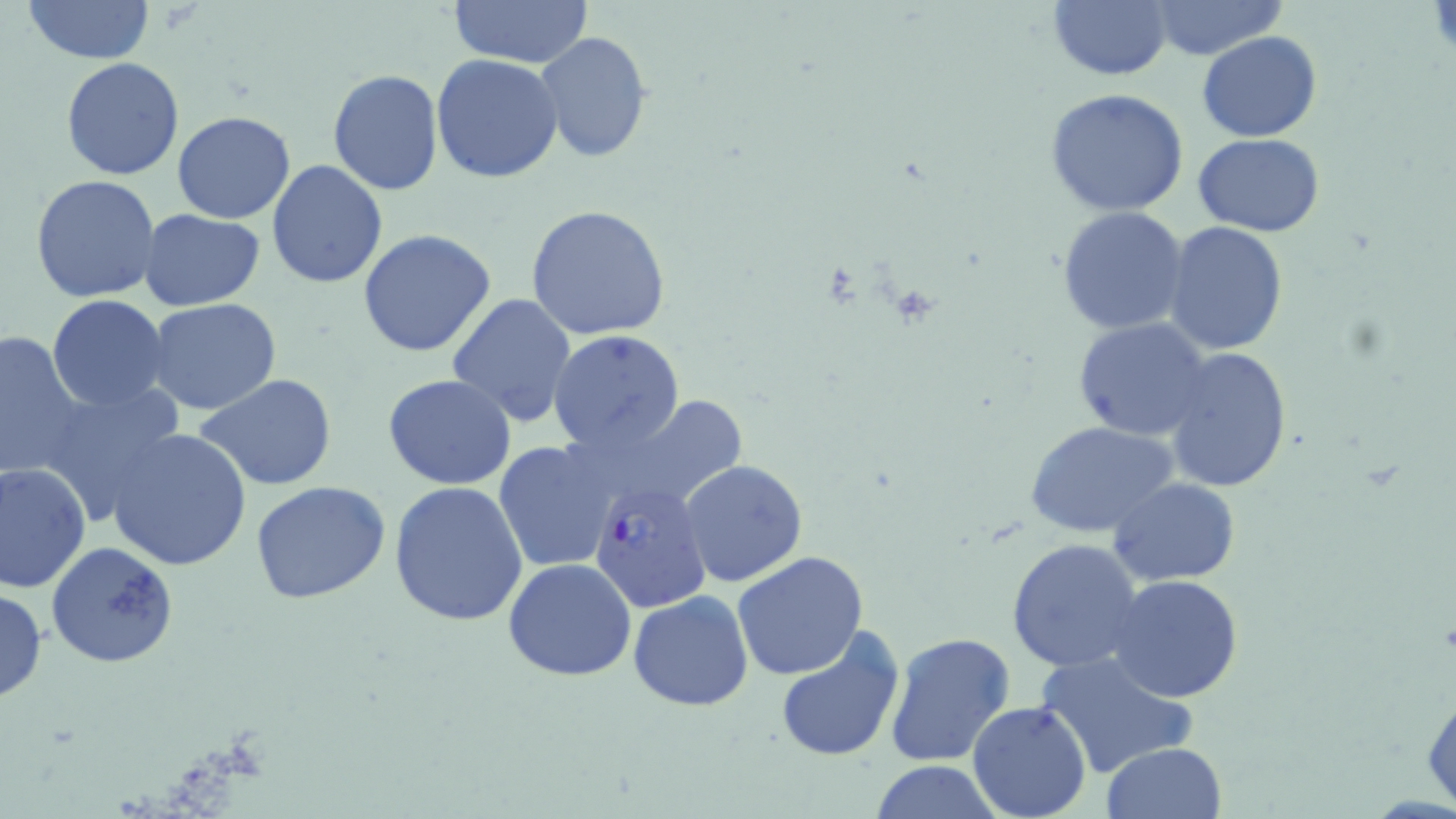

Approximate bounding boxes as named x1/y1/x2/y2 corners in pixels. Plasmodium falciparum-infected red blood cell locations: (x1=588, y1=479, x2=712, y2=614). Uninfected red blood cell locations: (x1=20, y1=0, x2=157, y2=65), (x1=449, y1=0, x2=593, y2=70), (x1=1049, y1=0, x2=1173, y2=81), (x1=1146, y1=3, x2=1283, y2=59), (x1=1197, y1=30, x2=1321, y2=142), (x1=532, y1=32, x2=653, y2=162), (x1=430, y1=53, x2=563, y2=182), (x1=60, y1=57, x2=186, y2=180), (x1=327, y1=69, x2=446, y2=196), (x1=1044, y1=88, x2=1189, y2=216), (x1=172, y1=111, x2=296, y2=224), (x1=1193, y1=133, x2=1324, y2=238), (x1=266, y1=158, x2=388, y2=289), (x1=31, y1=174, x2=162, y2=304), (x1=524, y1=203, x2=672, y2=342), (x1=1055, y1=207, x2=1189, y2=335), (x1=139, y1=208, x2=267, y2=311), (x1=1165, y1=222, x2=1287, y2=355), (x1=357, y1=229, x2=498, y2=357), (x1=446, y1=292, x2=578, y2=426), (x1=47, y1=294, x2=172, y2=413), (x1=146, y1=299, x2=283, y2=417), (x1=1074, y1=317, x2=1214, y2=442), (x1=0, y1=329, x2=88, y2=483), (x1=549, y1=330, x2=685, y2=454), (x1=1163, y1=347, x2=1292, y2=493), (x1=194, y1=373, x2=340, y2=493), (x1=384, y1=374, x2=517, y2=491), (x1=33, y1=378, x2=189, y2=524), (x1=591, y1=395, x2=747, y2=512), (x1=1026, y1=420, x2=1179, y2=539), (x1=107, y1=428, x2=253, y2=572), (x1=493, y1=440, x2=619, y2=574), (x1=679, y1=459, x2=808, y2=587), (x1=0, y1=462, x2=92, y2=593), (x1=1108, y1=478, x2=1242, y2=585), (x1=250, y1=481, x2=392, y2=605), (x1=389, y1=481, x2=529, y2=627), (x1=1006, y1=537, x2=1146, y2=673), (x1=46, y1=540, x2=179, y2=668), (x1=732, y1=552, x2=870, y2=682), (x1=503, y1=558, x2=638, y2=682), (x1=1109, y1=573, x2=1245, y2=702), (x1=0, y1=587, x2=48, y2=703), (x1=627, y1=592, x2=754, y2=711), (x1=773, y1=626, x2=906, y2=764), (x1=883, y1=632, x2=1016, y2=766), (x1=1035, y1=646, x2=1198, y2=779), (x1=1422, y1=677, x2=1455, y2=813), (x1=967, y1=701, x2=1093, y2=819), (x1=1101, y1=741, x2=1226, y2=819), (x1=867, y1=761, x2=1005, y2=818). Slide-level diagnosis: Plasmodium falciparum. Image is 1456×819 pixels. Single field of view. Thin blood smear. Light microscopy. May-Grünwald-Giemsa-stained preparation. Captured at 1000x magnification.